Assess this cell for malaria.
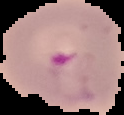

It is parasitized.

{
  "image_size": "124×115 pixels",
  "image_type": "segmented cell region on a black background",
  "preparation": "thin blood film"
}